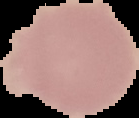

{
  "result": "no malaria parasites detected",
  "image_type": "segmented cell region with the area outside set to black",
  "preparation": "thin blood smear",
  "image_size": "139×118 pixels"
}